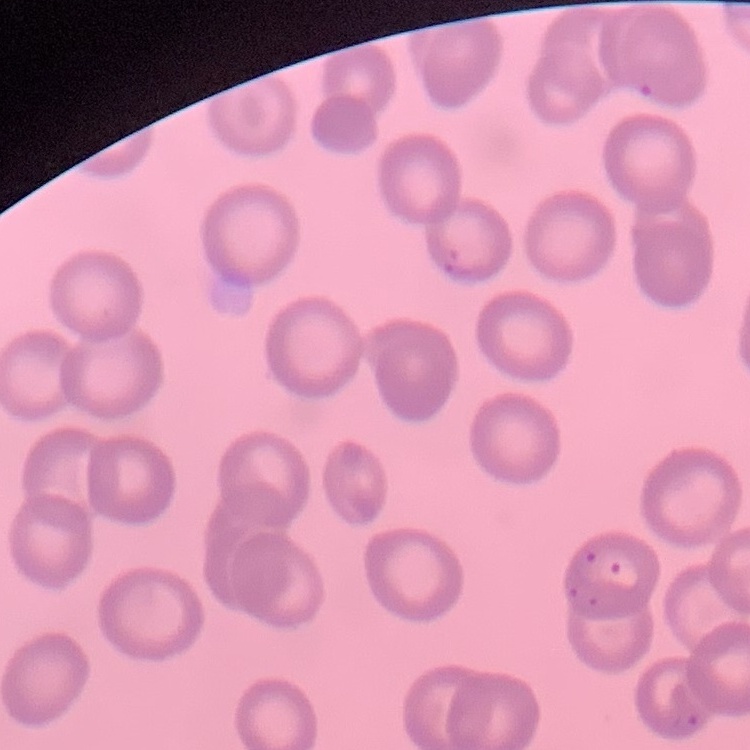

Summary:
  - Erythrocyte morphology: no rouleaux formation
  - Stain: Field's or Giemsa
  - Preparation: thin blood film
  - Image type: square crop of a larger photomicrograph